Name the parasite shown.
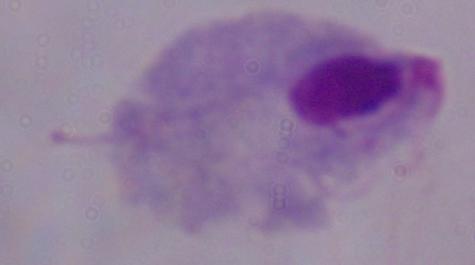
This is a trichomonad.

modality = photomicrograph
magnification = 1000x